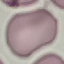

result = no malaria parasites seen
preparation = thin blood smear
stain = Giemsa
capture = smartphone camera at the microscope eyepiece
image type = automatically extracted cell patch, resized to 64 × 64 pixels